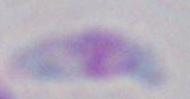 Captured at 1000x magnification. Toxoplasma gondii is shown. Micrograph.